Comment on the morphology of the erythrocytes.
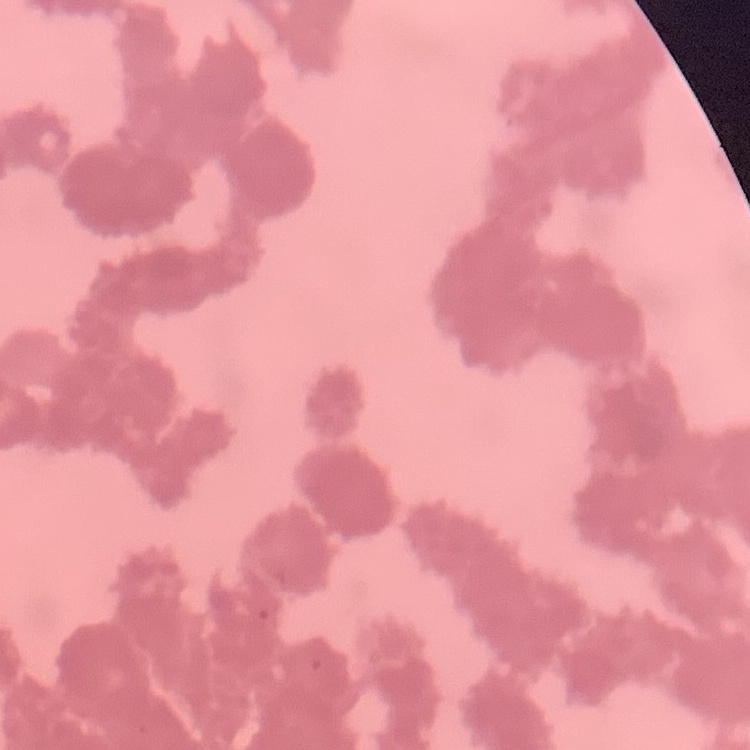
They show rouleaux formation.

preparation = thin blood film
stain = Field's or Giemsa
image type = one tile cut from a larger photomicrograph